Report the malaria status of this cell.
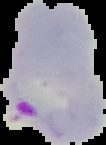

It is parasitized.

Summary:
  - Image size: 106×145 pixels
  - Preparation: thin blood film
  - Image type: segmented cell region on a black background